Classify this cell by malaria status.
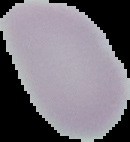
It is uninfected.

Cell region segmented out of the field of view; the surrounding area is masked to black. Image is 130×142 pixels. From a thin blood smear.